Name the blood parasite species.
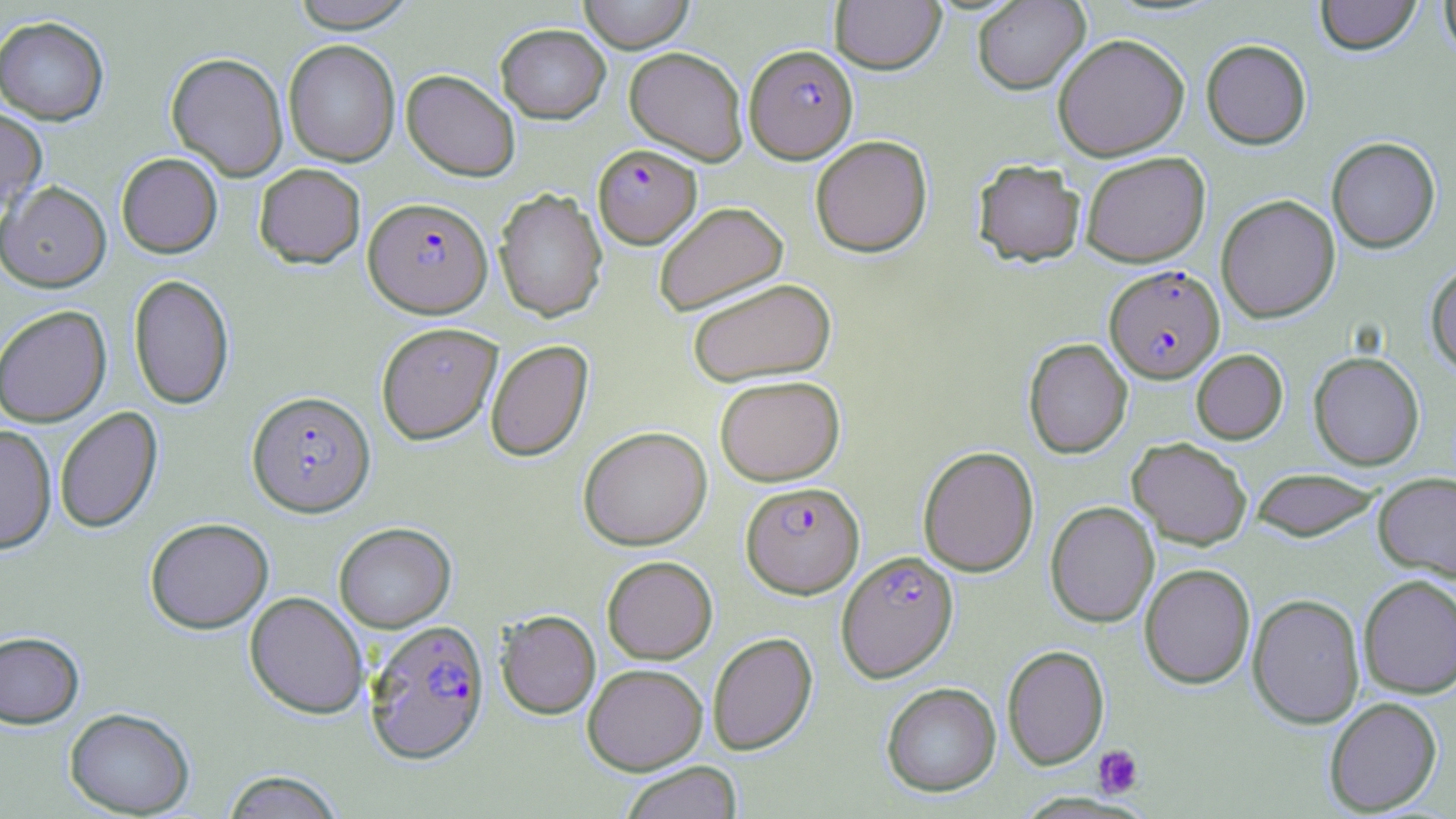
Plasmodium falciparum.

{
  "modality": "light microscopy",
  "preparation": "thin blood film",
  "magnification": "1000x",
  "image_size": "1456×819 pixels",
  "uninfected_red_blood_cell_locations": "approximate bounding boxes as named x1/y1/x2/y2 corners in pixels: (x1=289, y1=0, x2=417, y2=32), (x1=578, y1=0, x2=694, y2=53), (x1=830, y1=0, x2=945, y2=74), (x1=1315, y1=0, x2=1421, y2=55), (x1=1439, y1=0, x2=1456, y2=61), (x1=972, y1=1, x2=1090, y2=94), (x1=0, y1=15, x2=109, y2=125), (x1=495, y1=24, x2=610, y2=123), (x1=1052, y1=33, x2=1190, y2=161), (x1=283, y1=39, x2=400, y2=166), (x1=1201, y1=39, x2=1311, y2=149), (x1=624, y1=46, x2=748, y2=165), (x1=166, y1=51, x2=288, y2=181), (x1=402, y1=69, x2=520, y2=181), (x1=0, y1=107, x2=47, y2=212), (x1=810, y1=135, x2=932, y2=257), (x1=1326, y1=136, x2=1440, y2=253), (x1=1080, y1=151, x2=1211, y2=268), (x1=116, y1=152, x2=222, y2=258), (x1=973, y1=159, x2=1086, y2=266), (x1=253, y1=163, x2=366, y2=268), (x1=0, y1=180, x2=111, y2=292), (x1=494, y1=187, x2=608, y2=322), (x1=1216, y1=194, x2=1340, y2=323), (x1=653, y1=201, x2=788, y2=316), (x1=1425, y1=262, x2=1456, y2=377), (x1=128, y1=273, x2=234, y2=410), (x1=686, y1=277, x2=837, y2=387), (x1=0, y1=304, x2=112, y2=426), (x1=376, y1=321, x2=503, y2=444), (x1=1023, y1=338, x2=1132, y2=459), (x1=485, y1=339, x2=593, y2=462), (x1=1191, y1=349, x2=1288, y2=444), (x1=1308, y1=351, x2=1425, y2=470), (x1=715, y1=374, x2=845, y2=486), (x1=54, y1=406, x2=163, y2=534), (x1=0, y1=424, x2=57, y2=553), (x1=578, y1=425, x2=712, y2=551), (x1=1127, y1=437, x2=1253, y2=549), (x1=917, y1=445, x2=1040, y2=577), (x1=1251, y1=468, x2=1382, y2=541), (x1=1373, y1=471, x2=1456, y2=581), (x1=1045, y1=501, x2=1159, y2=627), (x1=145, y1=517, x2=274, y2=633), (x1=334, y1=522, x2=456, y2=632), (x1=602, y1=555, x2=717, y2=664), (x1=1139, y1=563, x2=1256, y2=689), (x1=1358, y1=574, x2=1456, y2=699), (x1=245, y1=591, x2=369, y2=719), (x1=1247, y1=593, x2=1366, y2=729), (x1=496, y1=610, x2=600, y2=719), (x1=0, y1=631, x2=84, y2=729), (x1=707, y1=632, x2=817, y2=755), (x1=1002, y1=644, x2=1109, y2=769), (x1=582, y1=663, x2=707, y2=774), (x1=881, y1=682, x2=1001, y2=797), (x1=1324, y1=697, x2=1442, y2=815), (x1=64, y1=707, x2=195, y2=817), (x1=620, y1=761, x2=743, y2=819), (x1=220, y1=769, x2=346, y2=818)",
  "field_of_view": "single",
  "stain": "May-Grünwald-Giemsa",
  "platelet_locations": "approximate bounding boxes as named x1/y1/x2/y2 corners in pixels: (x1=1093, y1=744, x2=1144, y2=797)",
  "plasmodium_falciparum_infected_red_blood_cell_locations": "approximate bounding boxes as named x1/y1/x2/y2 corners in pixels: (x1=744, y1=44, x2=858, y2=164), (x1=593, y1=143, x2=702, y2=248), (x1=363, y1=196, x2=493, y2=317), (x1=1104, y1=265, x2=1224, y2=383), (x1=246, y1=390, x2=376, y2=517), (x1=741, y1=481, x2=864, y2=598), (x1=836, y1=550, x2=958, y2=682), (x1=364, y1=619, x2=489, y2=764)"
}